State the preparation type.
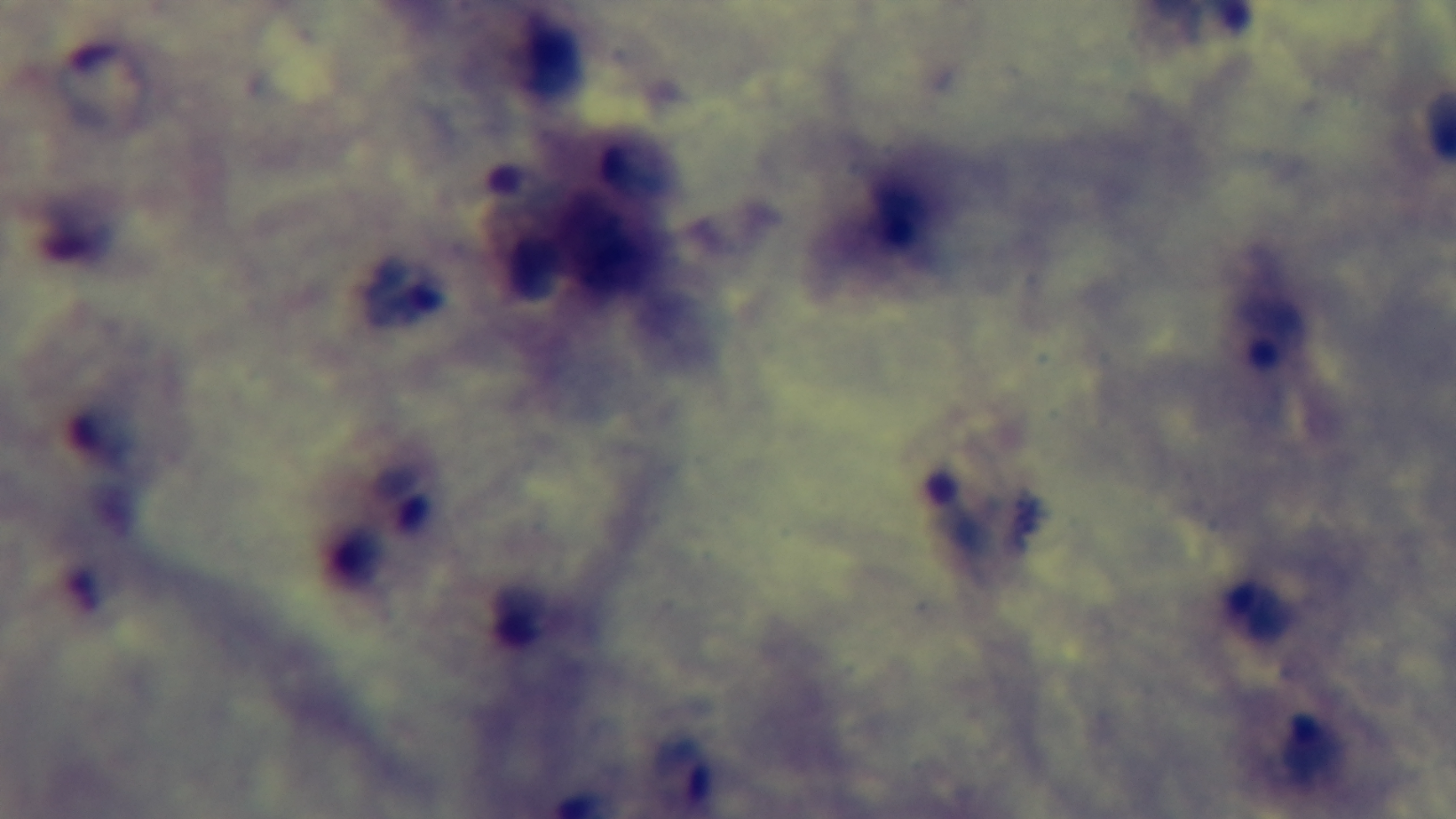

Thick.

Photomicrograph. Malaria status: positive. Oil-immersion objective, 100x. Giemsa-stained. Single field of view. Captured with a mounted 4K digital camera.